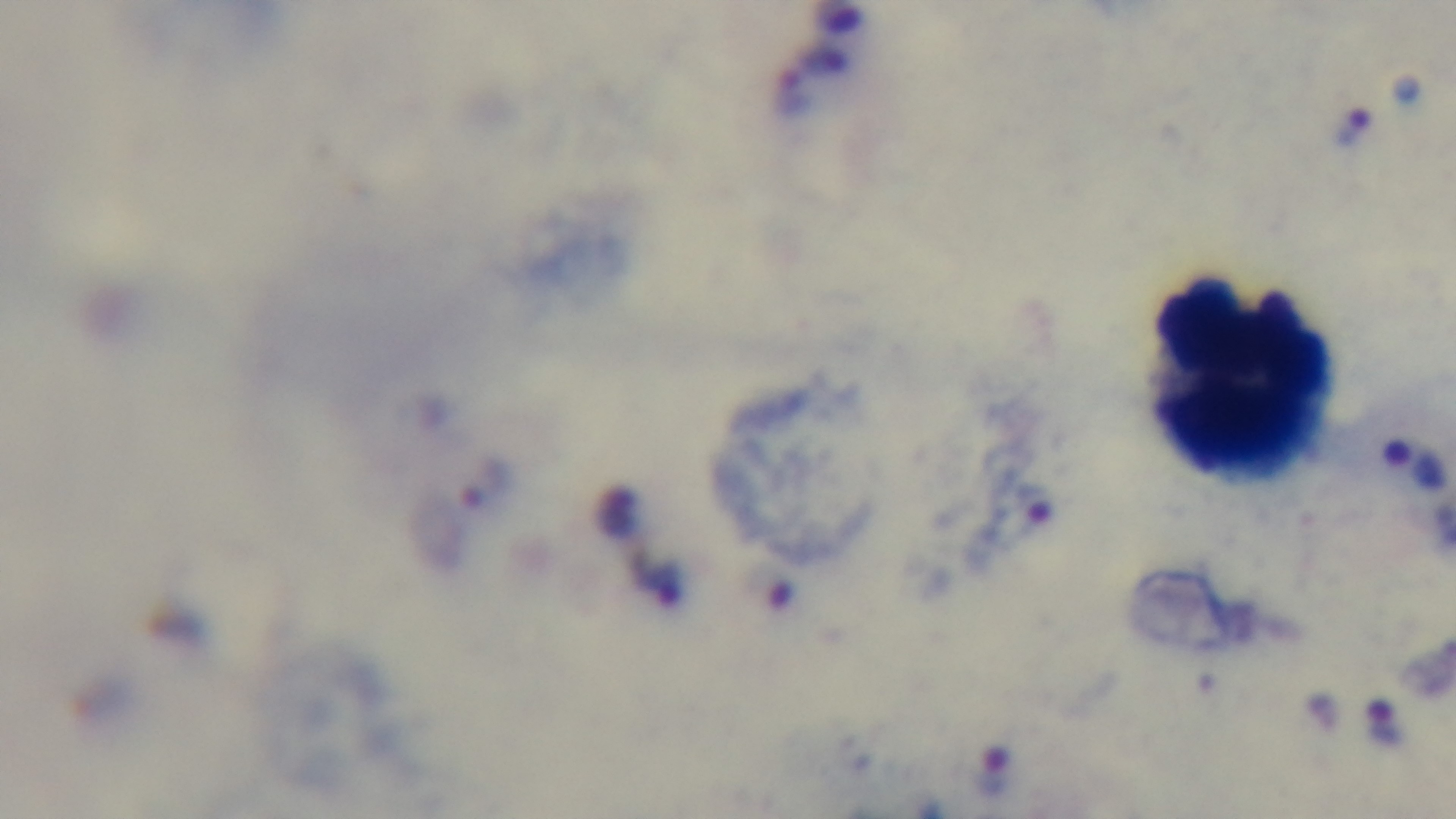
Summary:
  - Preparation: thick
  - Objective: 100x oil immersion
  - Stain: Giemsa
  - Modality: light microscopy
  - Capture: mounted 4K digital camera
  - Malaria status: positive
  - Field of view: one from the slide